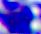

Summary:
  - Magnification: 400x
  - Identification: white blood cell
  - Modality: micrograph